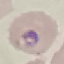

Summary:
  - Malaria status: parasitized
  - Capture: smartphone through the microscope eyepiece
  - Stain: Giemsa
  - Image type: cell patch, automatically extracted from a larger field of view and resized to 64 × 64 pixels
  - Preparation: thin blood smear